Locate Plasmodium parasites and leukocytes.
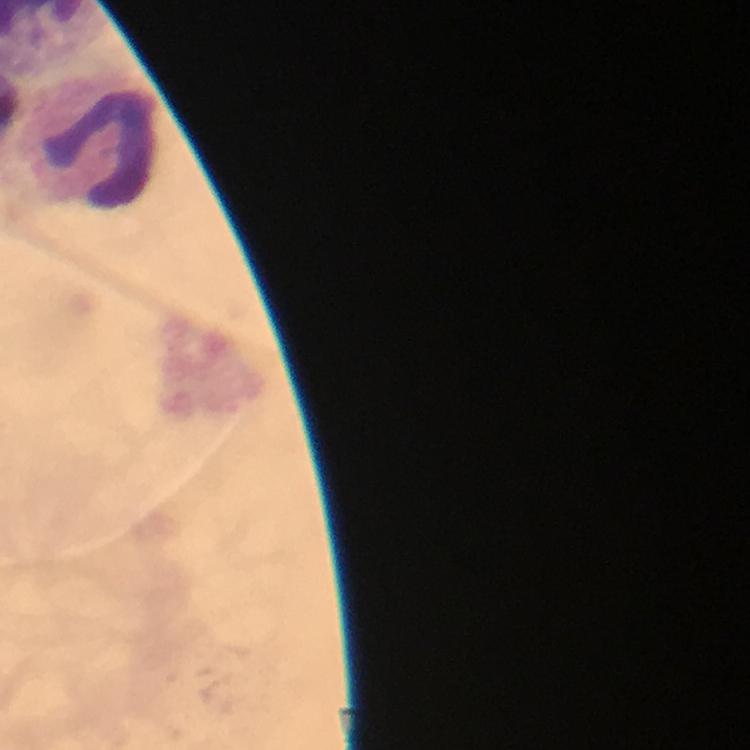

No Plasmodium parasites detected.
Approximate object centers, in pixels from the top-left corner.
Leukocytes: (x=94, y=143).

cropped from = a single field of view
image size = 750×750 pixels
preparation = thick smear
context = from a diagnostic examination for malaria
capture = smartphone mounted on the microscope
stain = Giemsa
immersion oil = applied
magnification = 100x